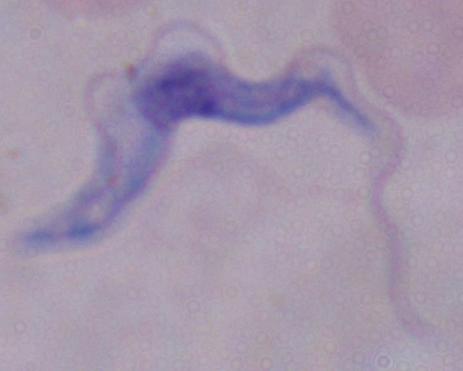

Summary:
  - Identification: trypanosome
  - Modality: micrograph
  - Magnification: 1000x